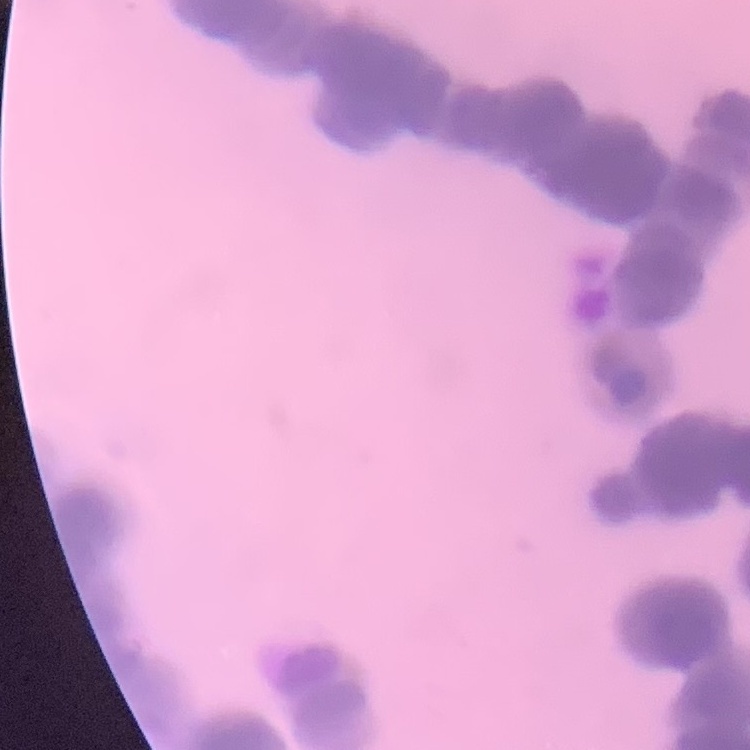
The erythrocytes exhibit rouleaux formation. Field's or Giemsa stain. Thin blood smear. One tile cut from a larger photomicrograph.